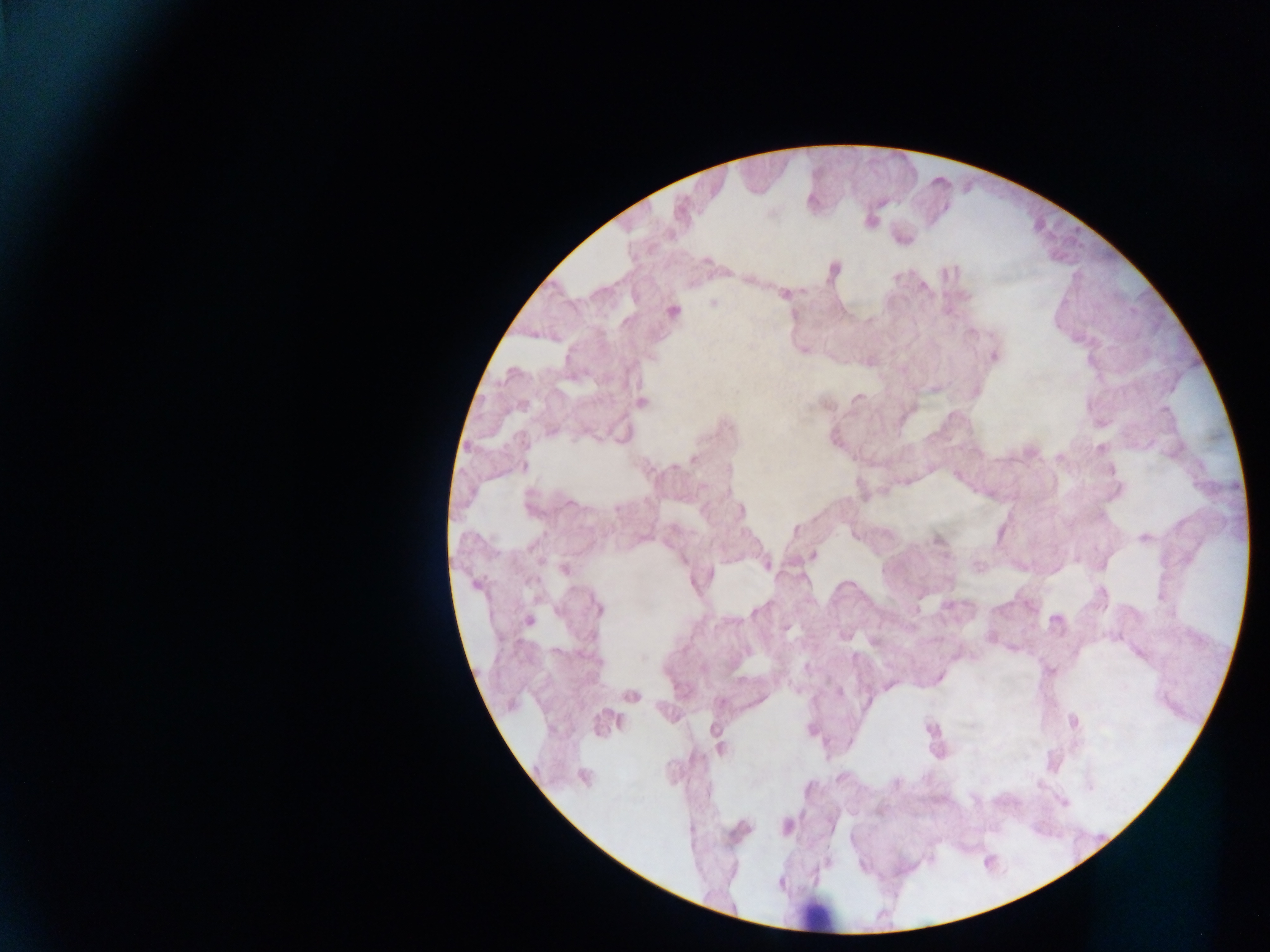
field of view = single
country = Ghana
preparation = thick blood smear
malaria parasite locations = approximate centers as [x, y] in pixels: [713, 303], [528, 621]
image size = 1270×952 pixels
leukocyte locations = approximate centers as [x, y] in pixels: [819, 915]
capture = mobile-phone photograph through a microscope